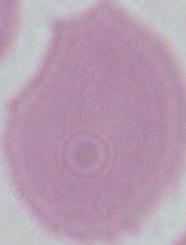
Summary:
  - Identification: erythrocyte
  - Modality: micrograph
  - Magnification: 1000x